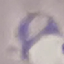

Summary:
  - Malaria status: parasitized
  - Preparation: thin blood film
  - Capture: smartphone camera at the microscope eyepiece
  - Stain: Giemsa
  - Image type: automatically extracted cell patch, resized to 64 × 64 pixels